Identify the blood parasite species.
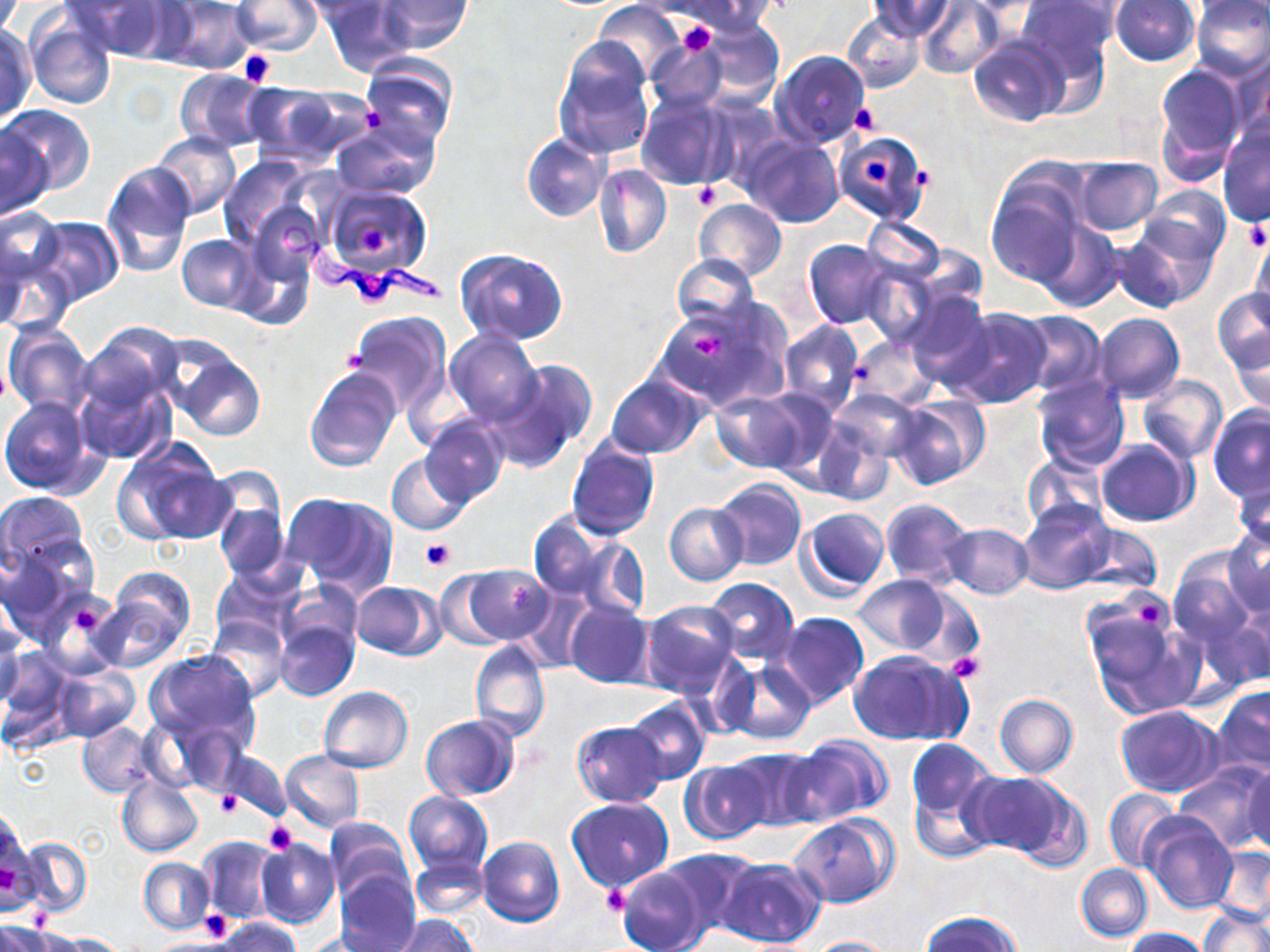
Trypanosoma brucei.

Approximate bounding boxes as (x1, y1, x2, y2) in pixels. Trypanosoma brucei locations: (283, 218, 446, 311). Uninfected red blood cell locations: (64, 0, 171, 59), (155, 0, 255, 74), (231, 0, 323, 54), (292, 0, 392, 23), (377, 0, 472, 52), (680, 0, 777, 35), (870, 0, 954, 41), (916, 0, 1004, 78), (1018, 0, 1119, 81), (321, 1, 417, 77), (1110, 1, 1199, 68), (1191, 1, 1269, 81), (1193, 3, 1268, 32), (593, 4, 686, 82), (843, 12, 925, 94), (26, 16, 117, 110), (694, 19, 783, 106), (0, 25, 36, 123), (968, 37, 1069, 127), (646, 39, 728, 112), (552, 40, 655, 159), (773, 51, 870, 149), (1226, 51, 1270, 144), (358, 58, 456, 150), (1154, 63, 1244, 177), (176, 67, 271, 152), (242, 81, 365, 165), (637, 95, 728, 191), (1, 104, 94, 194), (331, 117, 440, 200), (1217, 124, 1270, 227), (1, 125, 53, 219), (152, 132, 241, 218), (838, 132, 930, 223), (523, 134, 610, 223), (742, 134, 843, 228), (219, 155, 317, 251), (1072, 156, 1162, 235), (101, 161, 197, 276), (592, 164, 671, 258), (986, 177, 1085, 285), (321, 185, 432, 277), (1142, 185, 1230, 265), (694, 199, 786, 281), (246, 200, 326, 289), (2, 206, 64, 292), (29, 215, 124, 304), (863, 216, 949, 282), (1035, 219, 1122, 311), (1112, 221, 1214, 312), (1248, 228, 1270, 316), (178, 235, 260, 312), (234, 237, 318, 330), (804, 239, 896, 329), (0, 242, 74, 338), (455, 248, 569, 345), (671, 253, 759, 334), (859, 261, 941, 347), (1212, 286, 1270, 375), (904, 290, 992, 390), (654, 302, 783, 412), (947, 307, 1053, 409), (1013, 310, 1105, 398), (347, 311, 451, 417), (1091, 311, 1185, 404), (779, 320, 864, 415), (2, 321, 94, 416), (1224, 323, 1270, 415), (447, 332, 543, 426), (851, 334, 939, 409), (69, 341, 180, 464), (169, 351, 267, 442), (489, 359, 597, 474), (303, 366, 401, 472), (605, 374, 708, 460), (1138, 375, 1227, 463), (1031, 376, 1130, 473), (831, 389, 924, 465), (711, 391, 812, 473), (888, 395, 989, 490), (0, 396, 101, 496), (1207, 405, 1270, 503), (419, 416, 507, 506), (812, 418, 894, 506), (566, 437, 660, 539), (1097, 439, 1197, 526), (111, 441, 231, 546), (1022, 453, 1106, 530), (387, 454, 473, 535), (1230, 475, 1270, 556), (713, 479, 806, 571), (213, 489, 290, 584), (0, 490, 88, 576), (283, 493, 398, 597), (880, 498, 973, 589), (1018, 501, 1112, 595), (665, 503, 747, 585), (798, 507, 890, 599), (527, 510, 622, 603), (1075, 523, 1161, 593), (942, 524, 1034, 599), (1222, 526, 1270, 618), (568, 535, 649, 622), (0, 542, 93, 644), (1169, 553, 1258, 659), (462, 564, 555, 644), (100, 566, 195, 663), (209, 568, 297, 648), (433, 570, 513, 650), (853, 575, 954, 657), (703, 577, 798, 665), (350, 581, 445, 659), (280, 586, 363, 665), (40, 592, 119, 676), (1082, 597, 1204, 722), (1221, 597, 1270, 687), (563, 600, 653, 689), (637, 600, 738, 697), (775, 612, 869, 710), (204, 615, 289, 700), (273, 617, 358, 702), (0, 623, 25, 714), (3, 632, 44, 728), (469, 638, 551, 744), (0, 647, 76, 746), (145, 649, 259, 747), (848, 649, 972, 746), (721, 658, 816, 746), (54, 668, 140, 742), (318, 686, 413, 772), (1212, 686, 1270, 778), (995, 694, 1078, 778), (624, 698, 710, 785), (1115, 706, 1222, 796), (421, 715, 519, 799), (414, 716, 504, 877), (77, 720, 156, 797), (571, 720, 667, 806), (783, 736, 889, 828), (905, 738, 1001, 857), (725, 747, 823, 832), (220, 750, 291, 821), (280, 751, 365, 832), (680, 760, 772, 844), (1173, 760, 1268, 852), (1243, 763, 1270, 855), (964, 772, 1075, 861), (116, 773, 204, 857), (1104, 787, 1184, 872), (404, 791, 492, 878), (567, 797, 674, 893), (790, 813, 897, 908), (1141, 813, 1238, 914), (0, 814, 35, 914), (323, 817, 413, 902), (195, 834, 281, 925), (476, 836, 564, 927), (18, 838, 92, 919), (255, 838, 339, 929), (659, 847, 760, 936), (1210, 848, 1270, 924), (410, 855, 488, 919), (139, 857, 214, 935), (716, 857, 826, 948), (616, 863, 712, 952), (1076, 863, 1152, 941), (334, 866, 420, 951), (1200, 906, 1269, 952), (921, 911, 1022, 952), (395, 915, 477, 952), (212, 916, 299, 952), (1, 919, 56, 952), (1123, 927, 1213, 952), (44, 932, 126, 951), (299, 934, 382, 951), (800, 936, 902, 952). Platelet locations: (676, 22, 716, 56), (237, 47, 279, 86), (850, 104, 881, 136), (362, 107, 384, 130), (864, 159, 895, 185), (693, 183, 723, 210), (1244, 222, 1269, 251), (358, 224, 392, 256), (689, 331, 728, 360), (422, 538, 456, 570), (1136, 603, 1165, 628), (71, 604, 104, 635), (947, 653, 984, 681), (215, 790, 241, 817), (264, 822, 298, 853), (603, 885, 631, 915), (199, 909, 232, 940). One field of a larger specimen. Image is 1270×952 pixels. Thin blood film. Optical microscopy. May-Grünwald-Giemsa stain. Captured at 1000x magnification.